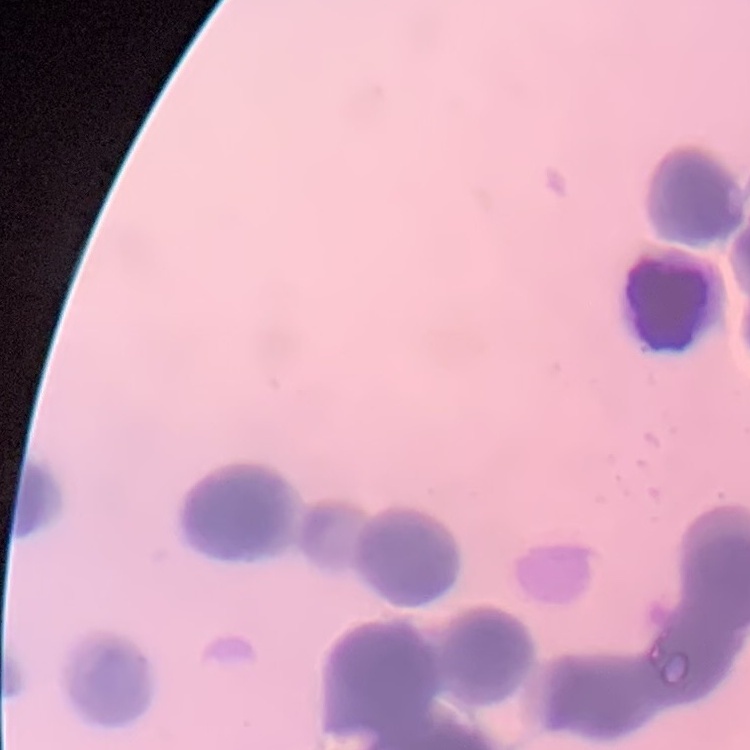
Summary:
  - Red blood cell morphology: rouleaux formation
  - Image type: square crop of a larger photomicrograph
  - Preparation: thin peripheral smear
  - Stain: Field's or Giemsa